Identify the parasite.
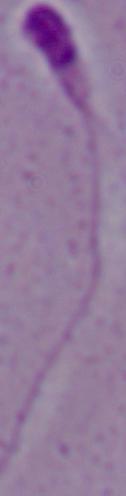

This is Leishmania.

Photomicrograph. 1000x magnification.